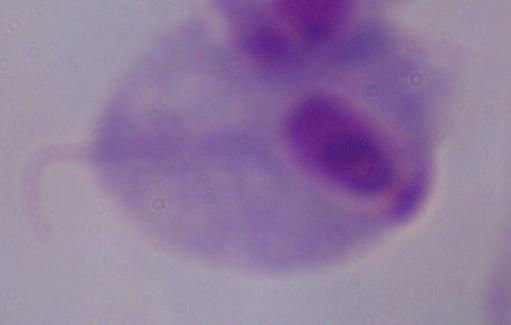

Summary:
  - Identification: trichomonad
  - Modality: micrograph
  - Magnification: 1000x